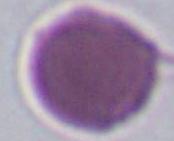

Summary:
  - Modality: photomicrograph
  - Magnification: 1000x
  - Identification: erythrocyte